Locate every blood parasite and identify its species.
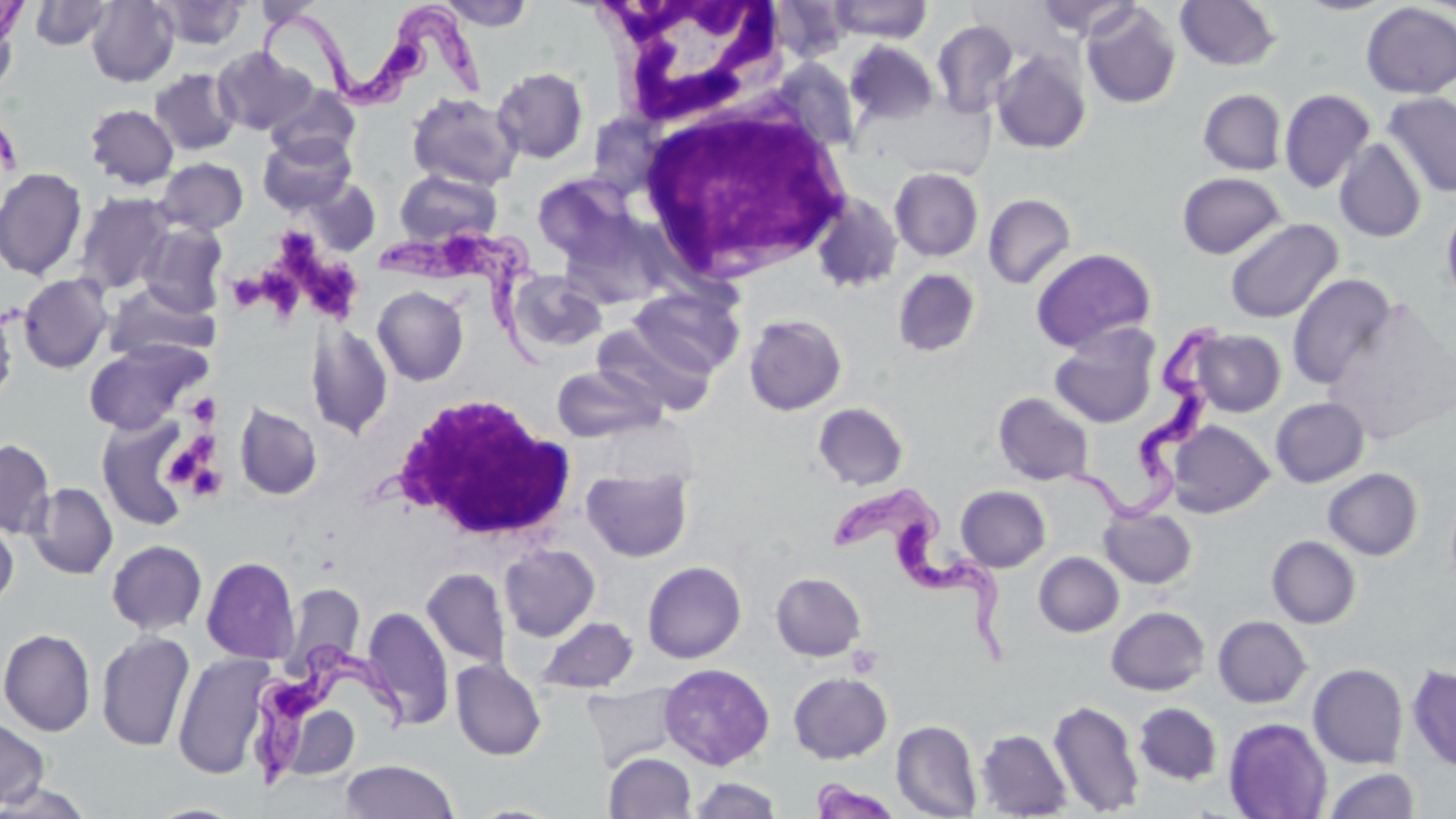
Approximate bounding boxes as [x1, y1, x2, y2] in pixels.
Trypanosoma brucei: [256, 0, 492, 111], [377, 223, 562, 371], [1066, 322, 1224, 521], [830, 489, 1014, 668], [247, 641, 413, 794].
No Plasmodium falciparum, Plasmodium ovale, Plasmodium malariae, Plasmodium vivax, or Babesia divergens observed.

{
  "slide_level_diagnosis": "Trypanosoma brucei",
  "uninfected_red_blood_cell_locations": "approximate bounding boxes as [x1, y1, x2, y2] in pixels: [0, 0, 29, 44], [86, 0, 179, 87], [827, 0, 933, 43], [1034, 0, 1141, 41], [1175, 0, 1281, 71], [29, 1, 114, 50], [152, 1, 248, 49], [437, 1, 535, 30], [1294, 1, 1395, 16], [1080, 2, 1181, 109], [1360, 2, 1456, 98], [0, 10, 19, 100], [931, 20, 1019, 118], [845, 40, 939, 125], [213, 47, 316, 136], [990, 49, 1092, 154], [492, 67, 589, 163], [150, 68, 240, 156], [266, 86, 361, 164], [1198, 88, 1287, 175], [1279, 88, 1376, 193], [407, 92, 523, 190], [1381, 92, 1456, 199], [86, 104, 178, 190], [259, 133, 355, 214], [1334, 139, 1426, 243], [155, 157, 248, 235], [0, 167, 87, 280], [889, 167, 984, 261], [395, 169, 502, 247], [1176, 171, 1286, 259], [300, 177, 380, 257], [73, 192, 175, 295], [811, 193, 903, 293], [983, 193, 1076, 289], [1441, 200, 1456, 313], [1224, 218, 1343, 324], [138, 222, 229, 317], [1030, 248, 1156, 351], [893, 267, 981, 357], [507, 271, 607, 354], [18, 273, 113, 373], [1286, 273, 1398, 390], [104, 283, 218, 363], [372, 285, 469, 386], [630, 287, 745, 378], [744, 314, 847, 415], [306, 320, 393, 439], [592, 323, 715, 417], [1048, 327, 1159, 428], [1191, 328, 1286, 417], [84, 341, 206, 435], [551, 365, 664, 443], [993, 392, 1094, 486], [1270, 397, 1369, 487], [234, 402, 322, 499], [813, 402, 908, 490], [97, 415, 192, 529], [1167, 421, 1274, 517], [0, 439, 55, 538], [581, 468, 694, 561], [1323, 468, 1423, 560], [26, 481, 118, 579], [957, 485, 1051, 572], [1099, 506, 1197, 588], [0, 516, 18, 610], [1267, 535, 1361, 628], [106, 539, 207, 635], [499, 544, 600, 642], [1034, 551, 1124, 637], [201, 556, 300, 664], [648, 560, 755, 769], [421, 567, 511, 670], [771, 572, 866, 660], [282, 584, 365, 673], [362, 606, 453, 729], [1106, 606, 1209, 695], [1213, 615, 1311, 708], [536, 617, 639, 694], [0, 628, 96, 736], [96, 630, 195, 752], [172, 652, 274, 779], [451, 660, 546, 760], [660, 663, 775, 769], [1308, 663, 1408, 768], [1407, 664, 1455, 772], [788, 671, 892, 763], [581, 683, 682, 771], [1048, 698, 1145, 816], [1133, 702, 1222, 785], [291, 710, 359, 782], [0, 715, 50, 810], [1224, 718, 1332, 819], [892, 720, 982, 818], [976, 729, 1071, 818], [604, 752, 697, 818], [340, 759, 459, 819], [1323, 767, 1420, 819], [687, 776, 783, 818], [809, 779, 904, 819], [0, 780, 94, 818]",
  "preparation": "thin blood film",
  "white_blood_cell_locations": "approximate bounding boxes as [x1, y1, x2, y2] in pixels: [600, 0, 789, 131], [632, 98, 855, 285], [390, 392, 580, 544]",
  "platelet_locations": "approximate bounding boxes as [x1, y1, x2, y2] in pixels: [276, 227, 319, 278], [307, 261, 357, 317], [260, 269, 299, 314], [236, 277, 267, 309], [187, 394, 220, 427], [190, 431, 217, 467], [169, 450, 200, 479], [192, 467, 221, 495]",
  "field_of_view": "one of a larger specimen",
  "image_size": "1456×819 pixels",
  "modality": "light microscopy",
  "magnification": "1000x",
  "stain": "May-Grünwald-Giemsa"
}